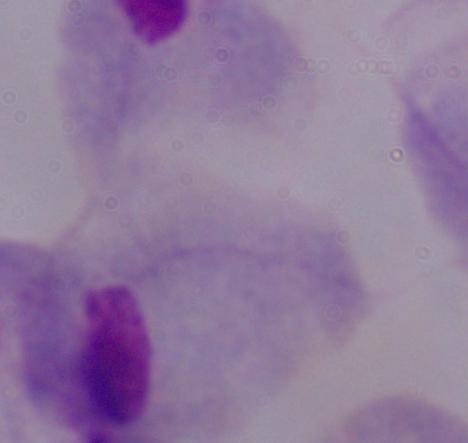
identification: trichomonad
magnification: 1000x
modality: photomicrograph